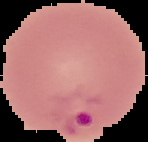
Summary:
  - Result: Plasmodium parasites detected
  - Image size: 148×142 pixels
  - Image type: cell region segmented out of the field of view; surrounding area masked to black
  - Preparation: thin blood film